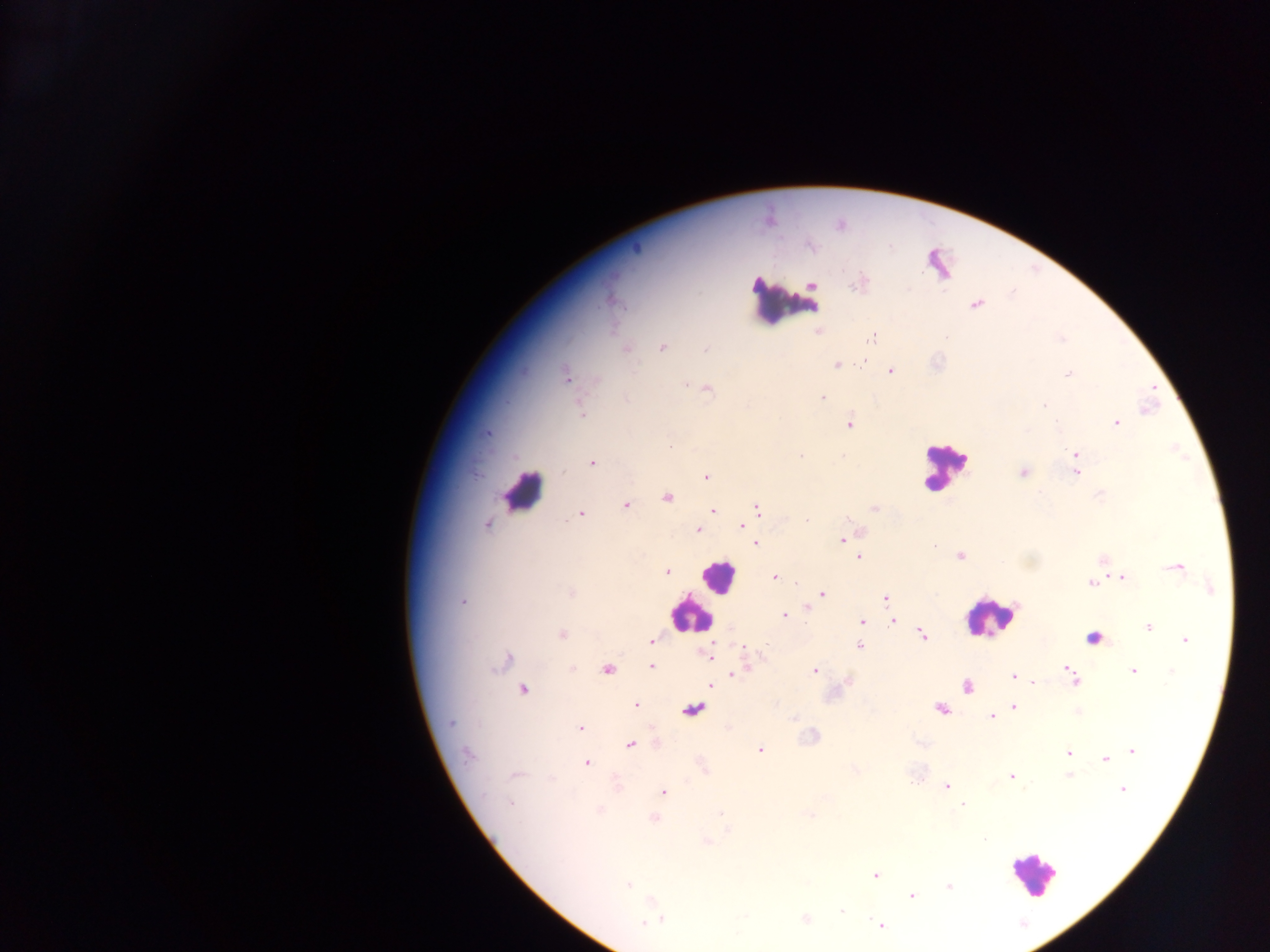 Approximate centers as [x, y] in pixels. Leukocyte locations: [786, 300], [945, 466], [523, 485], [716, 576], [689, 613], [989, 618], [1032, 873]. Plasmodium parasite locations: [811, 246], [857, 284], [612, 301], [976, 304], [819, 333], [871, 338], [663, 348], [625, 349], [706, 350], [863, 361], [837, 365], [891, 371], [1067, 374], [566, 376], [686, 385], [708, 390], [823, 397], [626, 399], [1044, 405], [581, 412], [1117, 423], [849, 424], [488, 432], [1075, 453], [801, 456], [843, 456], [592, 462], [1075, 462], [1022, 472], [1076, 472], [706, 477], [1100, 494], [667, 498], [626, 505], [874, 508], [759, 509], [713, 510], [580, 514], [806, 520], [487, 525], [742, 525], [698, 530], [843, 539], [756, 543], [934, 546], [960, 556], [859, 557], [1176, 568], [667, 572], [775, 577], [1122, 577], [1091, 583], [1211, 589], [571, 593], [823, 594], [885, 598], [463, 602], [808, 608], [785, 616], [862, 621], [893, 622], [1148, 627], [561, 634], [922, 635], [1093, 638], [652, 641], [1185, 641], [860, 647], [709, 655], [507, 660], [651, 667], [572, 669], [1068, 669], [607, 670], [815, 671], [1133, 671], [734, 675], [1013, 676], [1075, 680], [848, 682], [1034, 683], [710, 685], [967, 687], [524, 690], [635, 705], [1013, 706], [941, 708], [693, 710], [991, 716], [451, 722], [580, 728], [631, 745], [759, 749], [1132, 751], [467, 754], [1068, 754], [1109, 758], [1105, 759], [587, 763], [515, 775], [1068, 775], [1011, 777], [911, 782], [947, 787], [1122, 790], [664, 791], [510, 803], [962, 804], [600, 809], [720, 813], [810, 815], [654, 818], [984, 839], [707, 841], [875, 875], [628, 885], [949, 886], [912, 896], [842, 911], [661, 919], [805, 919], [653, 921], [645, 922], [880, 925]. Image is 1270×952 pixels. Sample from Ghana. Thick blood film. One field of view. Photographed through a microscope with a mobile-phone camera.